Report the malaria status of this cell.
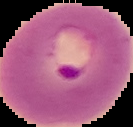
Parasitized.

Image is 133×127 pixels. Segmented cell region on a black background. From a thin blood smear.